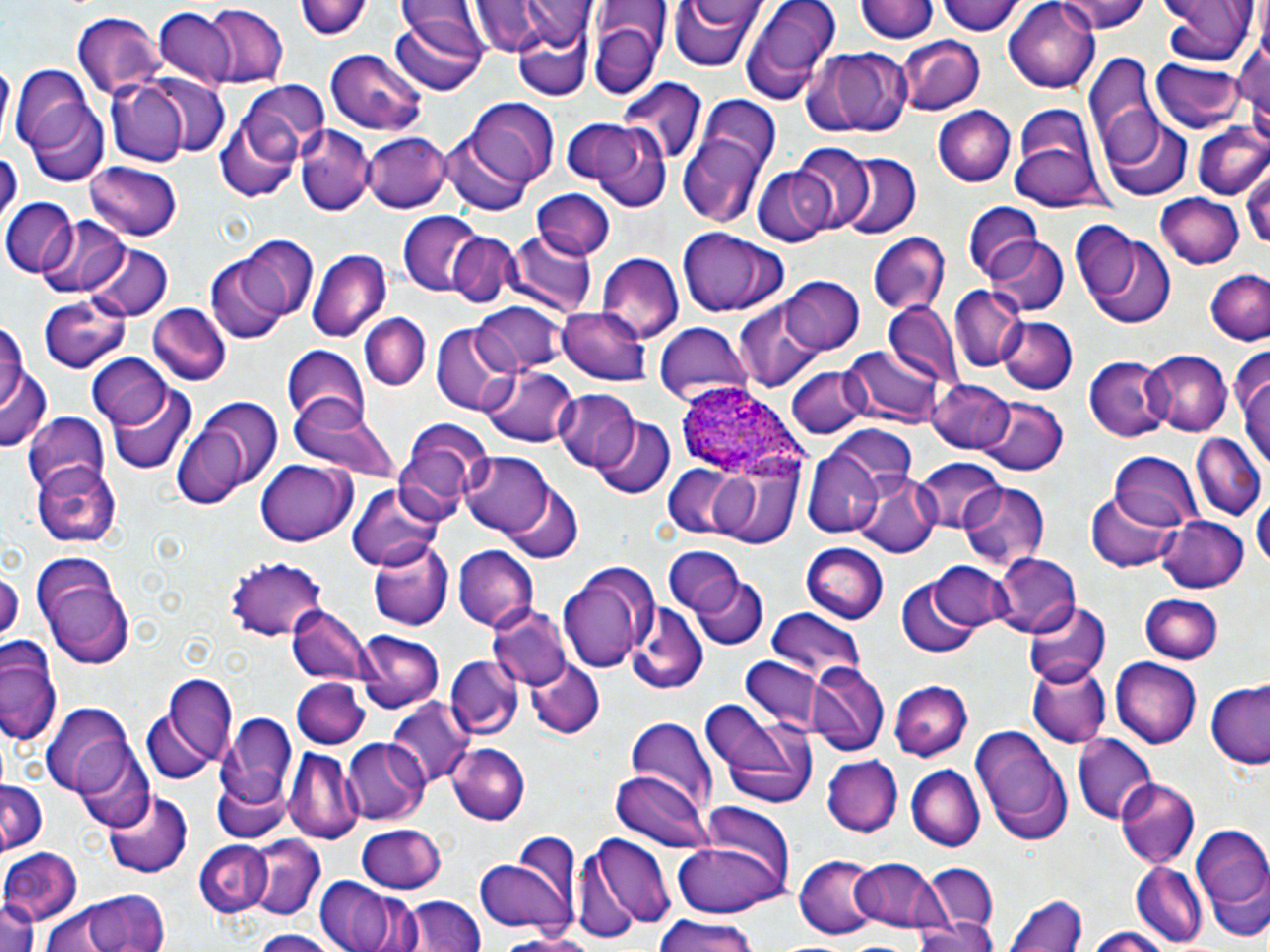

slide-level diagnosis = Plasmodium ovale
magnification = 1000x
field of view = one of a larger specimen
uninfected red blood cell locations = approximate bounding boxes as (x1, y1, x2, y2) in pixels: (298, 0, 374, 41), (469, 0, 578, 56), (670, 0, 761, 73), (736, 0, 844, 106), (855, 0, 937, 45), (939, 0, 1024, 38), (1005, 0, 1101, 90), (1058, 0, 1149, 33), (1160, 0, 1255, 69), (588, 2, 730, 88), (199, 4, 289, 88), (154, 10, 238, 87), (70, 12, 164, 99), (390, 14, 486, 95), (1233, 15, 1270, 131), (589, 20, 661, 100), (513, 23, 592, 99), (896, 36, 985, 115), (805, 46, 913, 138), (324, 49, 428, 137), (1084, 53, 1159, 162), (1150, 57, 1247, 136), (11, 64, 102, 159), (140, 72, 232, 159), (106, 77, 189, 164), (616, 78, 706, 167), (228, 81, 327, 186), (468, 99, 562, 186), (1011, 103, 1100, 196), (27, 104, 109, 187), (933, 105, 1016, 186), (675, 110, 778, 230), (214, 111, 304, 201), (1103, 117, 1191, 201), (569, 120, 672, 209), (1192, 121, 1270, 199), (294, 126, 375, 214), (442, 129, 531, 217), (362, 131, 453, 214), (790, 144, 874, 231), (0, 147, 20, 226), (836, 153, 921, 240), (86, 162, 181, 242), (1244, 163, 1270, 255), (753, 167, 833, 247), (532, 188, 615, 261), (1154, 194, 1244, 269), (2, 197, 78, 275), (962, 199, 1044, 278), (397, 211, 483, 295), (36, 214, 132, 298), (1084, 228, 1176, 327), (676, 229, 790, 319), (505, 231, 597, 318), (446, 233, 519, 309), (867, 234, 951, 312), (235, 235, 320, 321), (982, 237, 1068, 317), (79, 241, 175, 320), (308, 248, 390, 342), (597, 254, 684, 344), (206, 255, 292, 340), (1207, 270, 1270, 347), (778, 276, 865, 355), (949, 287, 1022, 373), (38, 298, 133, 373), (732, 299, 824, 394), (147, 303, 230, 385), (473, 304, 565, 375), (883, 304, 960, 387), (558, 305, 651, 384), (0, 311, 35, 437), (360, 312, 431, 390), (999, 316, 1076, 395), (652, 321, 754, 404), (430, 322, 519, 416), (282, 346, 370, 433), (843, 347, 942, 430), (1234, 347, 1269, 477), (1140, 350, 1231, 437), (89, 355, 171, 430), (1084, 358, 1171, 441), (482, 365, 579, 446), (787, 365, 869, 440), (928, 378, 1016, 454), (110, 384, 196, 474), (552, 389, 640, 473), (977, 396, 1067, 475), (171, 399, 282, 508), (290, 405, 405, 481), (22, 412, 113, 495), (594, 415, 674, 498), (395, 419, 491, 521), (831, 425, 918, 493), (1190, 433, 1266, 520), (803, 443, 890, 536), (459, 450, 554, 538), (1106, 453, 1200, 535), (708, 457, 805, 548), (255, 458, 358, 546), (913, 458, 1006, 533), (33, 461, 119, 546), (662, 464, 742, 539), (855, 473, 938, 558), (503, 482, 582, 562), (959, 482, 1050, 571), (348, 483, 444, 573), (1087, 489, 1180, 572), (1254, 496, 1269, 575), (1153, 513, 1250, 594), (367, 536, 453, 629), (803, 544, 889, 624), (661, 545, 745, 614), (452, 547, 538, 630), (992, 551, 1081, 639), (32, 555, 135, 668), (224, 556, 328, 641), (556, 560, 658, 674), (930, 562, 1016, 631), (0, 563, 21, 652), (691, 572, 768, 649), (896, 577, 984, 657), (1140, 593, 1223, 663), (1025, 598, 1110, 686), (626, 601, 707, 691), (489, 605, 572, 691), (288, 606, 371, 689), (766, 608, 866, 682), (355, 630, 445, 714), (0, 642, 62, 748), (446, 656, 521, 738), (524, 657, 605, 739), (1111, 658, 1200, 748), (740, 659, 825, 735), (808, 661, 890, 757), (1026, 663, 1110, 746), (162, 675, 238, 769), (292, 677, 367, 747), (887, 681, 971, 762), (1207, 684, 1270, 769), (698, 699, 818, 808), (387, 700, 473, 789), (42, 705, 137, 797), (217, 707, 299, 818), (143, 714, 215, 785), (621, 717, 718, 810), (970, 725, 1073, 843), (1072, 733, 1155, 824), (343, 739, 428, 825), (1092, 741, 1190, 846), (450, 742, 528, 824), (287, 747, 362, 843), (76, 749, 156, 833), (821, 755, 904, 836), (905, 763, 984, 849), (611, 770, 711, 852), (0, 779, 48, 857), (1115, 779, 1200, 869), (102, 789, 192, 878), (697, 801, 798, 899), (1191, 824, 1270, 922), (356, 825, 447, 894), (245, 834, 325, 919), (589, 834, 673, 932), (195, 840, 272, 919), (668, 841, 789, 918), (0, 848, 81, 925), (473, 854, 574, 937), (796, 854, 883, 938), (854, 858, 945, 933), (921, 863, 1000, 936), (1131, 863, 1205, 947), (312, 875, 416, 952), (61, 889, 176, 952), (1005, 889, 1086, 952), (401, 896, 488, 952), (1, 899, 40, 952), (37, 900, 135, 951), (652, 915, 761, 952), (908, 918, 999, 952), (1084, 927, 1177, 952), (495, 930, 606, 951), (247, 931, 344, 952)
preparation = thin blood smear
image size = 1270×952 pixels
Plasmodium ovale-infected red blood cell locations = approximate bounding boxes as (x1, y1, x2, y2) in pixels: (675, 387, 800, 474)
stain = May-Grünwald-Giemsa
modality = optical microscopy